Identify the blood parasite species.
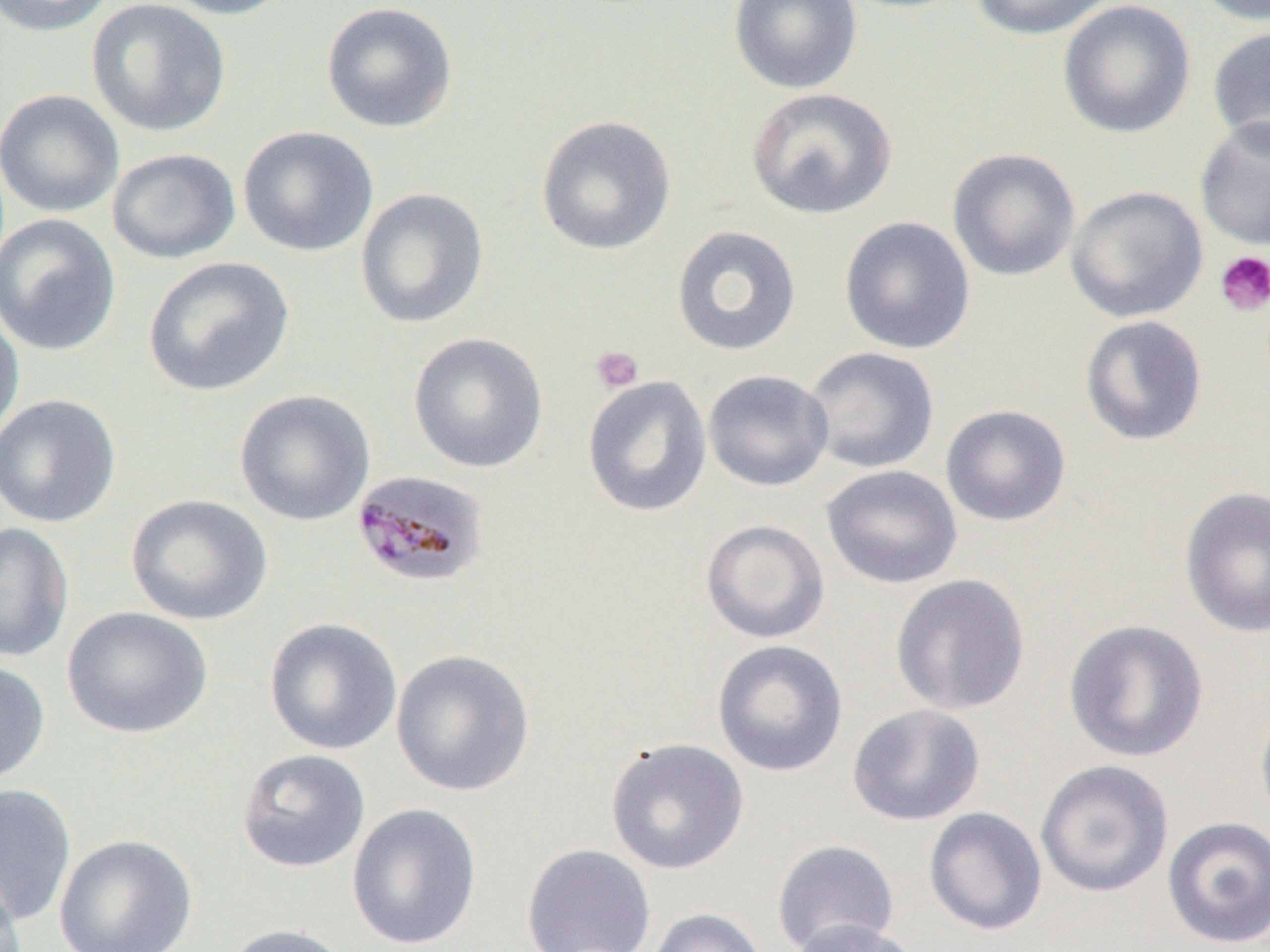

Plasmodium malariae.

Summary:
  - Coordinate format: approximate bounding boxes as named x1/y1/x2/y2 corners in pixels
  - Platelet locations: (x1=1214, y1=250, x2=1270, y2=316), (x1=590, y1=346, x2=644, y2=393)
  - Uninfected red blood cell locations: (x1=0, y1=0, x2=116, y2=37), (x1=86, y1=0, x2=232, y2=138), (x1=159, y1=0, x2=300, y2=19), (x1=728, y1=0, x2=862, y2=94), (x1=968, y1=0, x2=1117, y2=41), (x1=1189, y1=0, x2=1270, y2=26), (x1=320, y1=1, x2=459, y2=134), (x1=1057, y1=1, x2=1196, y2=139), (x1=1206, y1=25, x2=1270, y2=153), (x1=745, y1=87, x2=898, y2=220), (x1=0, y1=88, x2=125, y2=218), (x1=535, y1=115, x2=677, y2=256), (x1=1194, y1=116, x2=1270, y2=252), (x1=237, y1=125, x2=379, y2=258), (x1=106, y1=147, x2=241, y2=265), (x1=946, y1=148, x2=1081, y2=283), (x1=1066, y1=185, x2=1208, y2=323), (x1=355, y1=187, x2=489, y2=329), (x1=0, y1=213, x2=122, y2=357), (x1=838, y1=215, x2=976, y2=355), (x1=670, y1=225, x2=802, y2=357), (x1=143, y1=256, x2=295, y2=397), (x1=0, y1=298, x2=25, y2=444), (x1=1080, y1=315, x2=1208, y2=446), (x1=408, y1=332, x2=548, y2=473), (x1=803, y1=346, x2=940, y2=474), (x1=702, y1=369, x2=834, y2=492), (x1=582, y1=375, x2=712, y2=518), (x1=233, y1=389, x2=376, y2=525), (x1=0, y1=393, x2=122, y2=528), (x1=940, y1=404, x2=1072, y2=526), (x1=821, y1=464, x2=963, y2=590), (x1=1179, y1=485, x2=1269, y2=638), (x1=126, y1=494, x2=273, y2=626), (x1=700, y1=519, x2=830, y2=644), (x1=0, y1=521, x2=75, y2=662), (x1=890, y1=573, x2=1031, y2=716), (x1=62, y1=606, x2=213, y2=739), (x1=264, y1=617, x2=403, y2=756), (x1=1063, y1=618, x2=1210, y2=763), (x1=712, y1=640, x2=848, y2=777), (x1=390, y1=648, x2=536, y2=798), (x1=0, y1=659, x2=51, y2=788), (x1=1255, y1=691, x2=1270, y2=830), (x1=847, y1=704, x2=985, y2=826), (x1=605, y1=738, x2=749, y2=875), (x1=236, y1=748, x2=371, y2=873), (x1=1035, y1=759, x2=1175, y2=898), (x1=0, y1=783, x2=77, y2=928), (x1=347, y1=802, x2=482, y2=950), (x1=923, y1=807, x2=1048, y2=936), (x1=1161, y1=816, x2=1270, y2=949), (x1=54, y1=834, x2=198, y2=952), (x1=771, y1=839, x2=900, y2=951), (x1=521, y1=844, x2=657, y2=952), (x1=0, y1=870, x2=26, y2=952), (x1=647, y1=908, x2=769, y2=952), (x1=786, y1=919, x2=922, y2=952), (x1=220, y1=923, x2=354, y2=952)
  - Plasmodium malariae-infected red blood cell locations: (x1=351, y1=469, x2=490, y2=589)
  - Preparation: thin blood smear
  - Modality: light microscopy
  - Magnification: 1000x
  - Field of view: single
  - Image size: 1270×952 pixels